Classify this cell by malaria status.
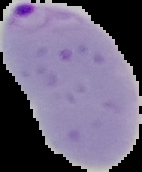

Parasitized.

Summary:
  - Image type: segmented cell region on a black background
  - Preparation: thin blood smear
  - Image size: 142×172 pixels